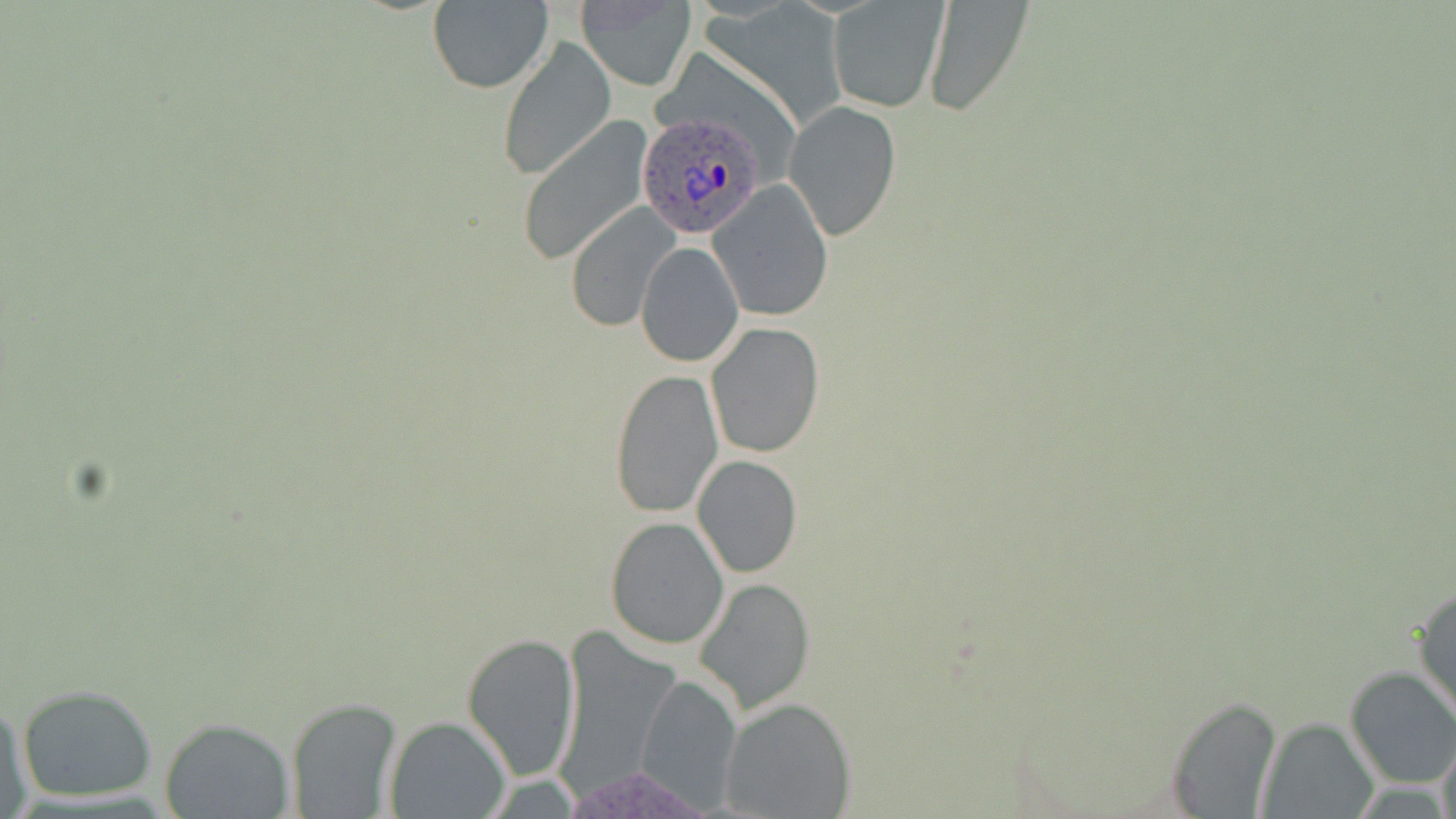

Approximate bounding boxes as [x1, y1, x2, y2] in pixels. Plasmodium ovale-infected red blood cell locations: [635, 113, 769, 237]. Uninfected red blood cell locations: [428, 0, 553, 93], [575, 0, 698, 91], [924, 1, 1033, 116], [826, 3, 946, 113], [497, 36, 616, 181], [784, 100, 901, 242], [516, 117, 653, 264], [708, 180, 835, 322], [565, 202, 681, 331], [634, 240, 744, 367], [705, 321, 825, 459], [609, 368, 723, 518], [692, 456, 803, 578], [605, 516, 728, 648], [695, 576, 815, 712], [1413, 584, 1456, 724], [462, 632, 580, 780], [1344, 666, 1456, 790], [636, 671, 742, 810], [17, 684, 160, 802], [1161, 693, 1284, 816], [721, 697, 857, 819], [286, 698, 405, 818], [1, 701, 33, 819], [383, 715, 510, 817], [159, 716, 295, 818], [1256, 717, 1380, 818], [1437, 733, 1455, 819]. Slide-level diagnosis: Plasmodium ovale. Captured at 1000x magnification. Image is 1456×819 pixels. May-Grünwald-Giemsa-stained preparation. One field of a larger specimen. Thin blood smear. Light microscopy.